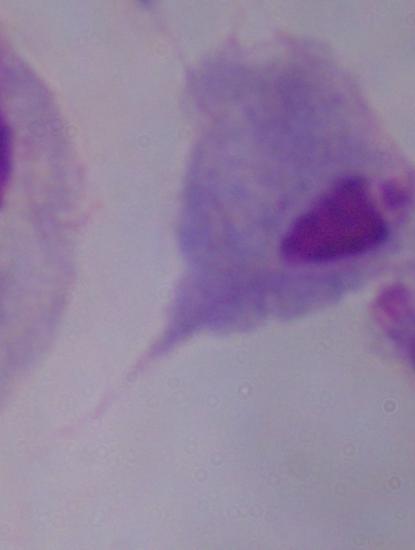
Summary:
  - Modality: micrograph
  - Identification: trichomonad
  - Magnification: 1000x